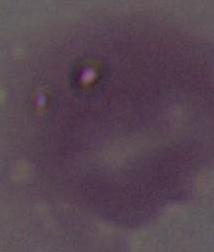

Summary:
  - Identification: erythrocyte
  - Modality: micrograph
  - Magnification: 1000x